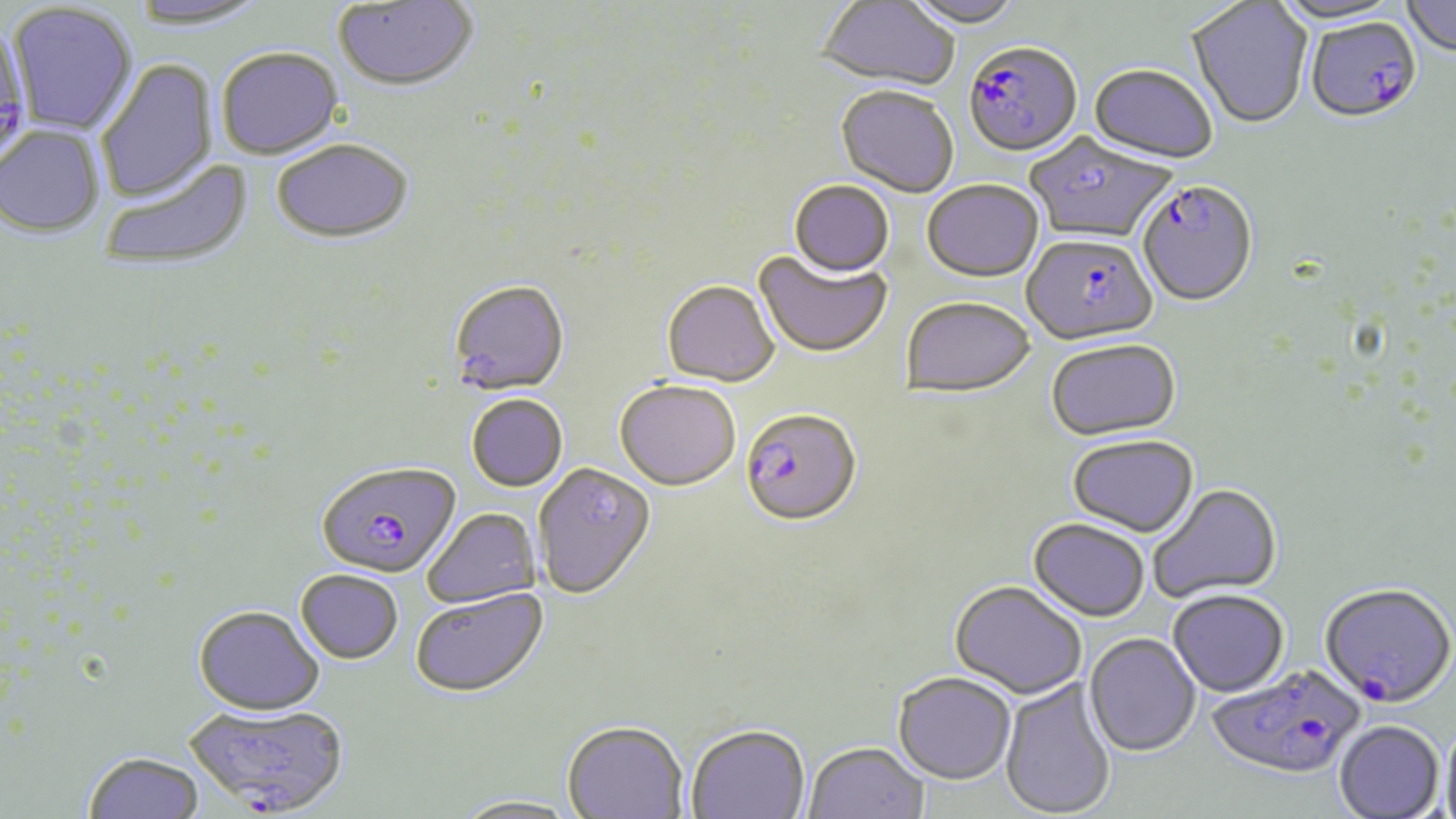
Summary:
  - Coordinate format: approximate bounding boxes as (x1,y1)-(x2,y2) corner pairs in pixels
  - Plasmodium falciparum-infected red blood cell locations: (1305,18)-(1422,126), (0,22)-(35,176), (964,44)-(1082,160), (1136,183)-(1259,309), (1023,234)-(1157,349), (739,410)-(862,531), (317,463)-(461,581), (1319,585)-(1455,710), (1205,664)-(1367,780), (185,704)-(350,816)
  - Uninfected red blood cell locations: (126,0)-(270,31), (816,0)-(960,95), (901,0)-(1025,31), (1272,0)-(1408,28), (1401,0)-(1456,59), (333,1)-(478,95), (1187,2)-(1313,131), (8,3)-(138,137), (217,50)-(344,162), (96,59)-(218,204), (1088,66)-(1218,167), (836,88)-(958,199), (0,126)-(104,239), (1026,133)-(1178,245), (272,141)-(413,248), (100,159)-(253,272), (788,182)-(895,280), (922,182)-(1044,285), (753,251)-(892,360), (447,281)-(570,399), (662,282)-(780,389), (901,298)-(1037,401), (1046,341)-(1182,442), (614,382)-(740,493), (467,396)-(568,493), (1066,436)-(1199,539), (534,464)-(657,602), (1147,484)-(1282,604), (422,508)-(542,609), (1027,519)-(1150,622), (296,572)-(402,665), (949,581)-(1087,700), (410,590)-(549,700), (1167,590)-(1290,698), (192,607)-(325,718), (1084,633)-(1201,757), (892,673)-(1016,785), (1000,678)-(1117,819), (1441,719)-(1456,819), (1334,720)-(1444,819), (562,724)-(688,819), (685,726)-(810,819), (804,744)-(928,819), (83,753)-(205,819), (451,797)-(583,819)
  - Slide-level diagnosis: Plasmodium falciparum
  - Magnification: 1000x
  - Stain: May-Grünwald-Giemsa
  - Modality: optical microscopy
  - Preparation: thin blood smear
  - Image size: 1456×819 pixels
  - Field of view: single